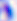
Toxoplasma gondii is seen. Micrograph. Captured at 400x magnification.